Give the preparation type.
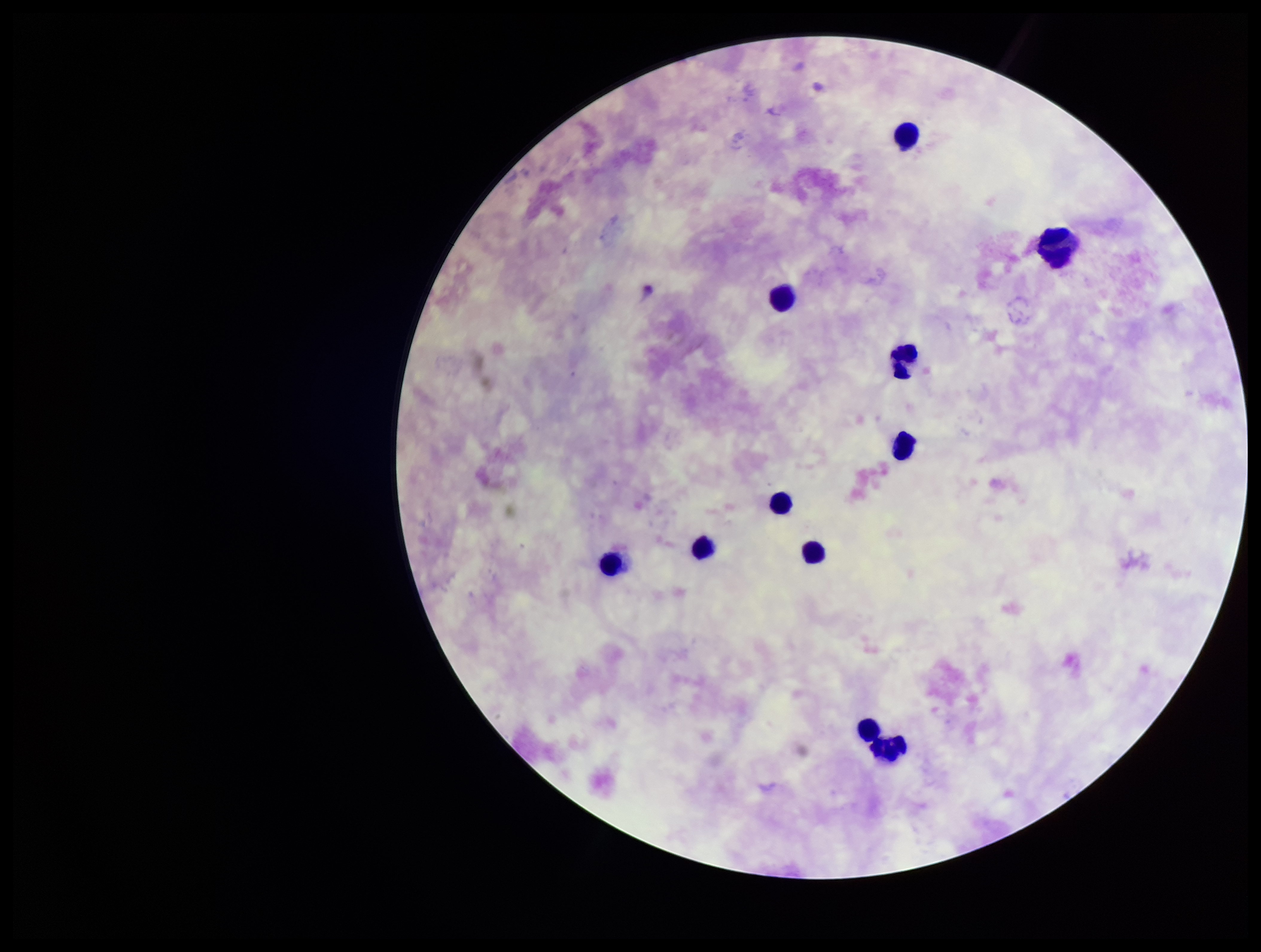
A thick smear.

Single field of view. Giemsa stain. Plasmodium parasites: none identified. Smartphone photograph taken through the eyepiece of a microscope. Patient malaria status: negative. Parasite count: 0. Leukocyte count: 11. Image is 1261×952 pixels.